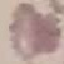
{
  "malaria_status": "uninfected",
  "stain": "Giemsa",
  "image_type": "automatically extracted cell patch, resized to 64 × 64 pixels",
  "preparation": "thin smear",
  "capture": "smartphone camera at the microscope eyepiece"
}